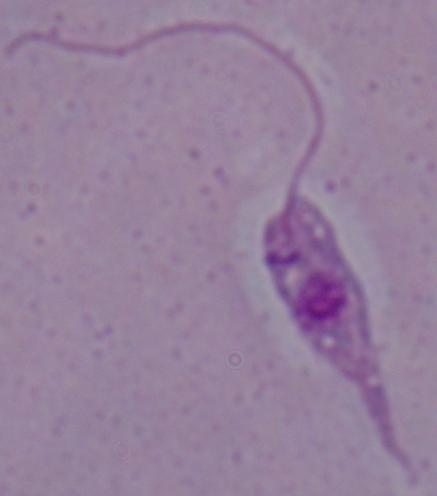

1000x magnification. Micrograph. A Leishmania parasite is seen.